Report the malaria status of this cell.
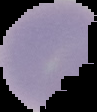
Uninfected.

image size = 97×112 pixels
preparation = thin blood smear
image type = segmented cell region on a black background